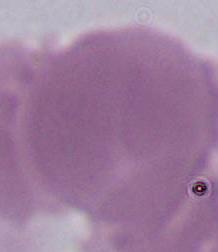
identification = red blood cell
magnification = 1000x
modality = micrograph